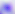

Summary:
  - Magnification: 400x
  - Identification: Toxoplasma gondii
  - Modality: micrograph